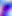
Toxoplasma gondii is shown. Captured at 400x magnification. Photomicrograph.